Locate every blood parasite and identify its species.
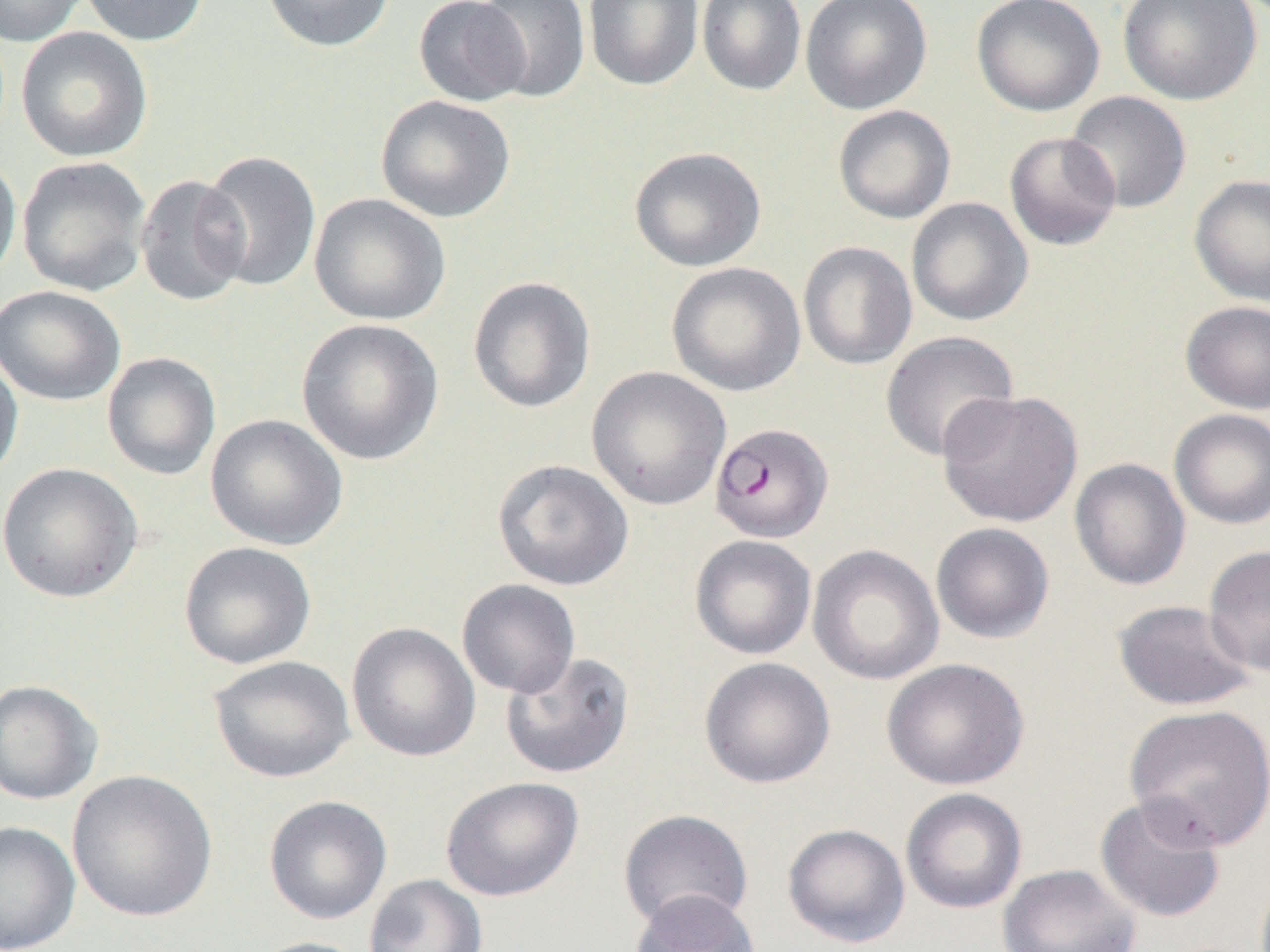

Approximate bounding boxes as (x1, y1, x2, y2) in pixels.
Plasmodium falciparum-infected red blood cells: (710, 422, 833, 543).
No Plasmodium ovale, Plasmodium malariae, Plasmodium vivax, Babesia divergens, or Trypanosoma brucei observed.

slide_level_diagnosis: Plasmodium falciparum
uninfected_red_blood_cell_locations: 'approximate bounding boxes as (x1, y1, x2, y2) in pixels: (0, 0, 89, 46), (80, 0, 209, 46), (260, 0, 395, 53), (413, 0, 532, 106), (474, 0, 591, 102), (583, 0, 703, 91), (697, 0, 807, 96), (800, 0, 932, 115), (971, 0, 1105, 116), (1117, 0, 1263, 106), (16, 26, 153, 162), (1064, 91, 1191, 214), (375, 95, 516, 223), (832, 105, 956, 224), (1004, 131, 1122, 251), (629, 146, 766, 272), (197, 150, 322, 292), (0, 151, 22, 287), (16, 156, 151, 296), (134, 174, 252, 306), (1189, 174, 1270, 307), (309, 193, 451, 325), (906, 198, 1033, 326), (798, 241, 917, 370), (665, 262, 806, 396), (467, 276, 596, 413), (0, 285, 126, 406), (1180, 300, 1270, 414), (297, 318, 444, 466), (879, 330, 1019, 462), (0, 348, 24, 485), (102, 351, 221, 480), (586, 366, 731, 511), (936, 389, 1083, 527), (1168, 409, 1270, 529), (205, 413, 348, 551), (1069, 458, 1190, 591), (492, 459, 634, 591), (0, 461, 143, 603), (930, 522, 1055, 643), (690, 535, 817, 660), (179, 541, 317, 669), (807, 544, 944, 685), (1203, 544, 1270, 677), (456, 579, 581, 698), (1112, 598, 1258, 711), (346, 622, 481, 763), (500, 650, 636, 779), (208, 655, 355, 783), (698, 656, 835, 789), (881, 658, 1030, 791), (0, 679, 102, 805), (1123, 703, 1270, 851), (67, 769, 218, 923), (440, 776, 585, 902), (900, 788, 1028, 914), (1094, 794, 1227, 923), (264, 795, 392, 925), (618, 808, 753, 931), (0, 820, 80, 952), (781, 823, 910, 948), (997, 863, 1141, 952), (364, 874, 488, 952), (629, 888, 759, 951), (245, 936, 372, 952)'
magnification: 1000x
field_of_view: single
image_size: 1270×952 pixels
modality: light microscopy
preparation: thin blood film